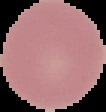 Image is 106×112 pixels. Cell region segmented out of the field of view; the surrounding area is masked to black. From a thin blood film. Result: negative for Plasmodium parasites.